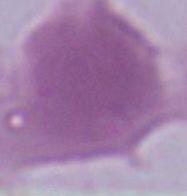

Summary:
  - Magnification: 1000x
  - Identification: red blood cell
  - Modality: micrograph